Identify the parasite.
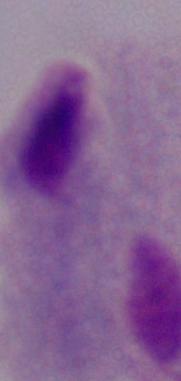
This is a trichomonad.

Micrograph. 1000x magnification.